Outline each Plasmodium malariae-infected red blood cell.
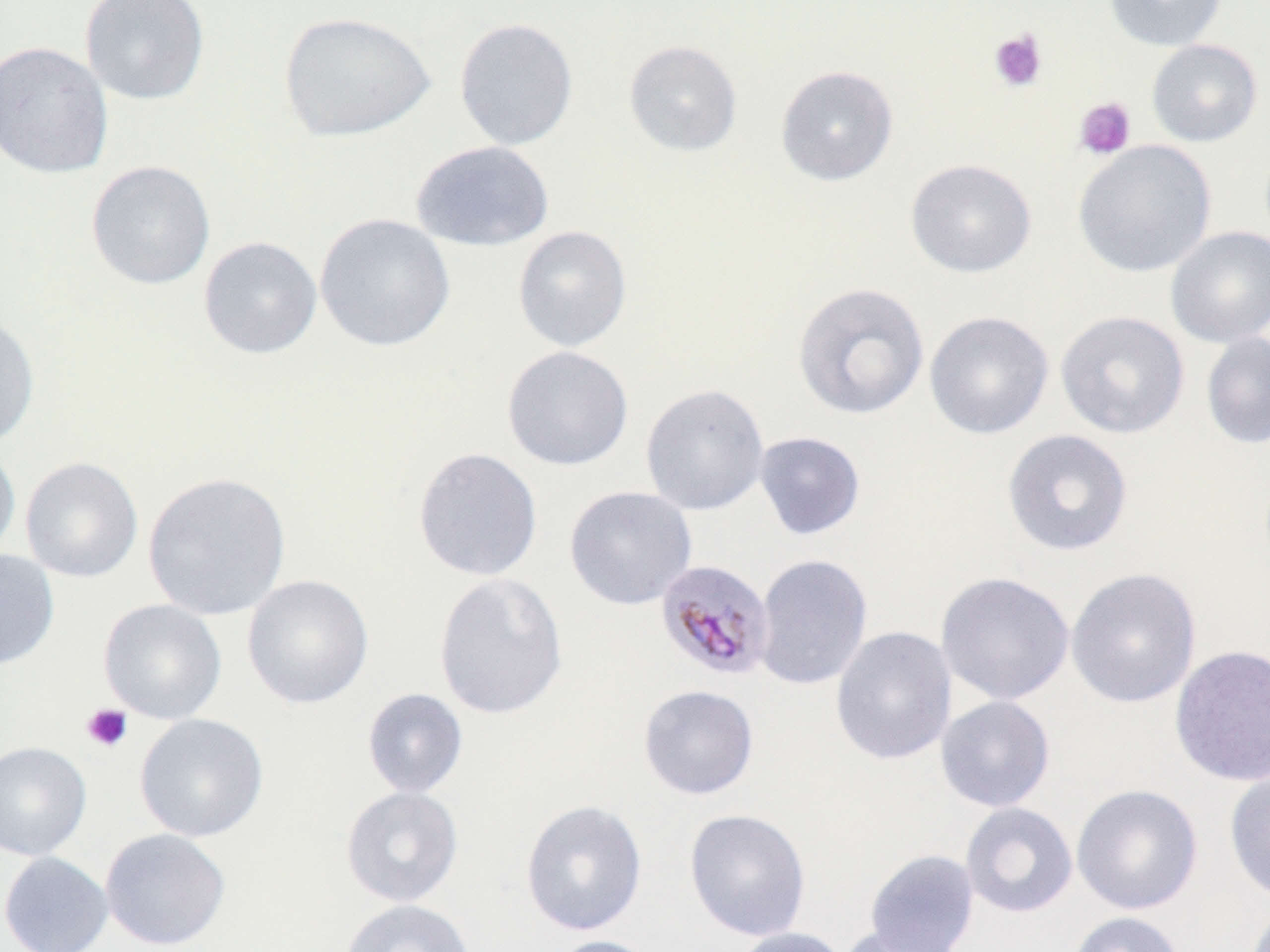

Approximate bounding boxes as (x1, y1, x2, y2) in pixels.
Plasmodium malariae-infected red blood cells: (655, 559, 776, 681).

Uninfected red blood cell locations: (80, 0, 210, 106), (1104, 0, 1228, 51), (278, 11, 435, 142), (453, 17, 579, 151), (1146, 39, 1263, 147), (0, 40, 113, 179), (622, 40, 743, 157), (775, 64, 899, 186), (410, 140, 554, 252), (1073, 140, 1218, 278), (905, 158, 1037, 278), (85, 160, 216, 290), (314, 213, 455, 352), (512, 226, 632, 352), (1165, 226, 1270, 347), (197, 236, 323, 360), (792, 282, 930, 420), (0, 310, 40, 449), (924, 310, 1054, 440), (1055, 310, 1190, 439), (1201, 332, 1270, 451), (501, 345, 634, 471), (640, 383, 770, 515), (1001, 429, 1134, 557), (754, 431, 866, 540), (0, 441, 21, 565), (412, 447, 543, 582), (20, 457, 143, 583), (141, 471, 293, 621), (564, 485, 697, 610), (0, 548, 60, 670), (753, 553, 872, 691), (1065, 568, 1201, 708), (432, 571, 569, 721), (935, 571, 1075, 705), (241, 574, 374, 709), (97, 598, 227, 724), (830, 625, 957, 765), (1169, 644, 1270, 787), (637, 684, 759, 800), (361, 688, 468, 799), (935, 695, 1056, 812), (134, 713, 269, 843), (0, 741, 92, 861), (1224, 767, 1270, 903), (1071, 783, 1203, 915), (340, 786, 463, 907), (520, 799, 648, 937), (960, 802, 1078, 918), (683, 808, 811, 941), (99, 828, 231, 950), (864, 848, 980, 952), (0, 851, 113, 952), (339, 898, 476, 952), (1066, 911, 1185, 952), (836, 925, 963, 952), (730, 926, 851, 952), (544, 935, 665, 952). Platelet locations: (989, 28, 1048, 93), (1073, 97, 1136, 161), (80, 704, 133, 753). Slide-level diagnosis: Plasmodium malariae. Thin blood smear. Image is 1270×952 pixels. One field of a larger specimen. May-Grünwald-Giemsa-stained preparation. Light microscopy. Captured at 1000x magnification.